Locate and identify every blood parasite.
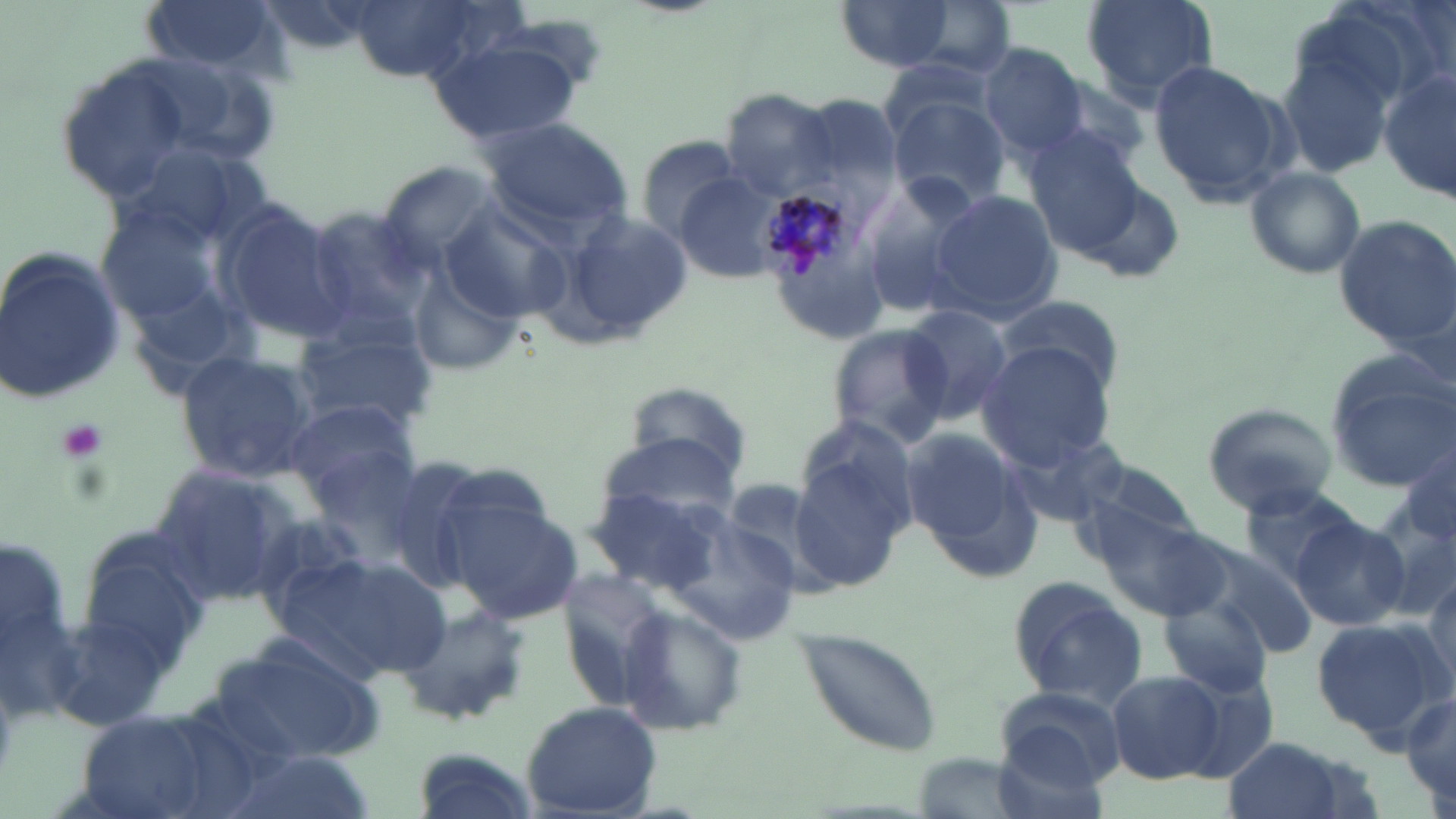
Approximate bounding boxes as (x1,y1)-(x2,y2) corner pairs in pixels.
Plasmodium malariae-infected red blood cells: (753,178)-(868,291).
No Plasmodium falciparum, Plasmodium ovale, Plasmodium vivax, Babesia divergens, or Trypanosoma brucei observed.

Platelet locations: (51,415)-(113,470). Uninfected red blood cell locations: (142,0)-(281,71), (342,0)-(498,82), (1081,0)-(1218,107), (835,1)-(955,72), (898,2)-(1015,79), (426,35)-(586,147), (981,42)-(1086,156), (1278,43)-(1405,181), (1147,59)-(1291,206), (54,62)-(195,199), (1378,66)-(1453,205), (1046,77)-(1158,174), (718,88)-(839,199), (887,93)-(1013,211), (482,117)-(634,235), (1021,126)-(1144,252), (638,136)-(745,244), (380,159)-(503,272), (1243,165)-(1367,279), (674,172)-(792,280), (857,173)-(977,315), (926,189)-(1062,323), (442,201)-(571,322), (214,205)-(355,346), (303,206)-(438,340), (547,208)-(696,348), (1334,215)-(1456,352), (0,248)-(127,406), (404,260)-(524,379), (994,295)-(1126,391), (900,304)-(1015,426), (290,322)-(437,437), (826,326)-(955,447), (976,339)-(1118,467), (174,350)-(317,481), (1326,359)-(1456,491), (620,380)-(755,487), (283,399)-(421,512), (1203,402)-(1337,515), (1003,426)-(1127,527), (790,431)-(916,593), (303,433)-(427,558), (904,433)-(1036,572), (593,434)-(738,535), (1398,436)-(1456,562), (376,455)-(489,588), (1077,463)-(1198,553), (148,465)-(305,602), (1238,483)-(1361,585), (587,485)-(730,592), (449,501)-(583,623), (1089,504)-(1230,624), (1292,515)-(1411,632), (1,523)-(78,729), (72,529)-(212,669), (1192,542)-(1318,660), (293,552)-(454,680), (1423,558)-(1456,686), (1009,579)-(1146,709), (1161,597)-(1270,695), (399,602)-(532,728), (620,607)-(749,735), (41,614)-(170,730), (1310,615)-(1447,742), (797,628)-(942,753), (210,631)-(386,767), (1105,669)-(1221,786), (1173,671)-(1280,782), (996,687)-(1128,792), (1401,690)-(1456,812), (522,702)-(662,817), (71,708)-(228,819), (1224,735)-(1356,819), (990,736)-(1111,819), (407,745)-(539,819). Slide-level diagnosis: Plasmodium malariae. May-Grünwald-Giemsa stain. Light microscopy. Image is 1456×819 pixels. Captured at 1000x magnification. Thin blood film. Single field of view.